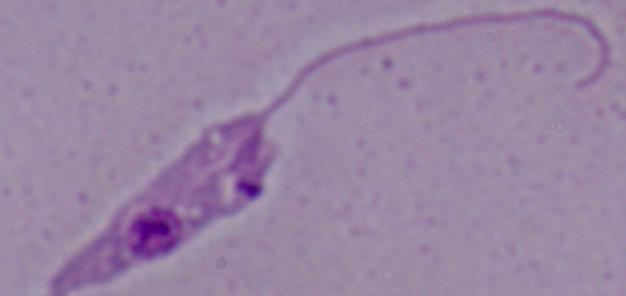

{
  "magnification": "1000x",
  "modality": "micrograph",
  "identification": "Leishmania"
}